Give the extent of all Plasmodium ovale-infected red blood cells.
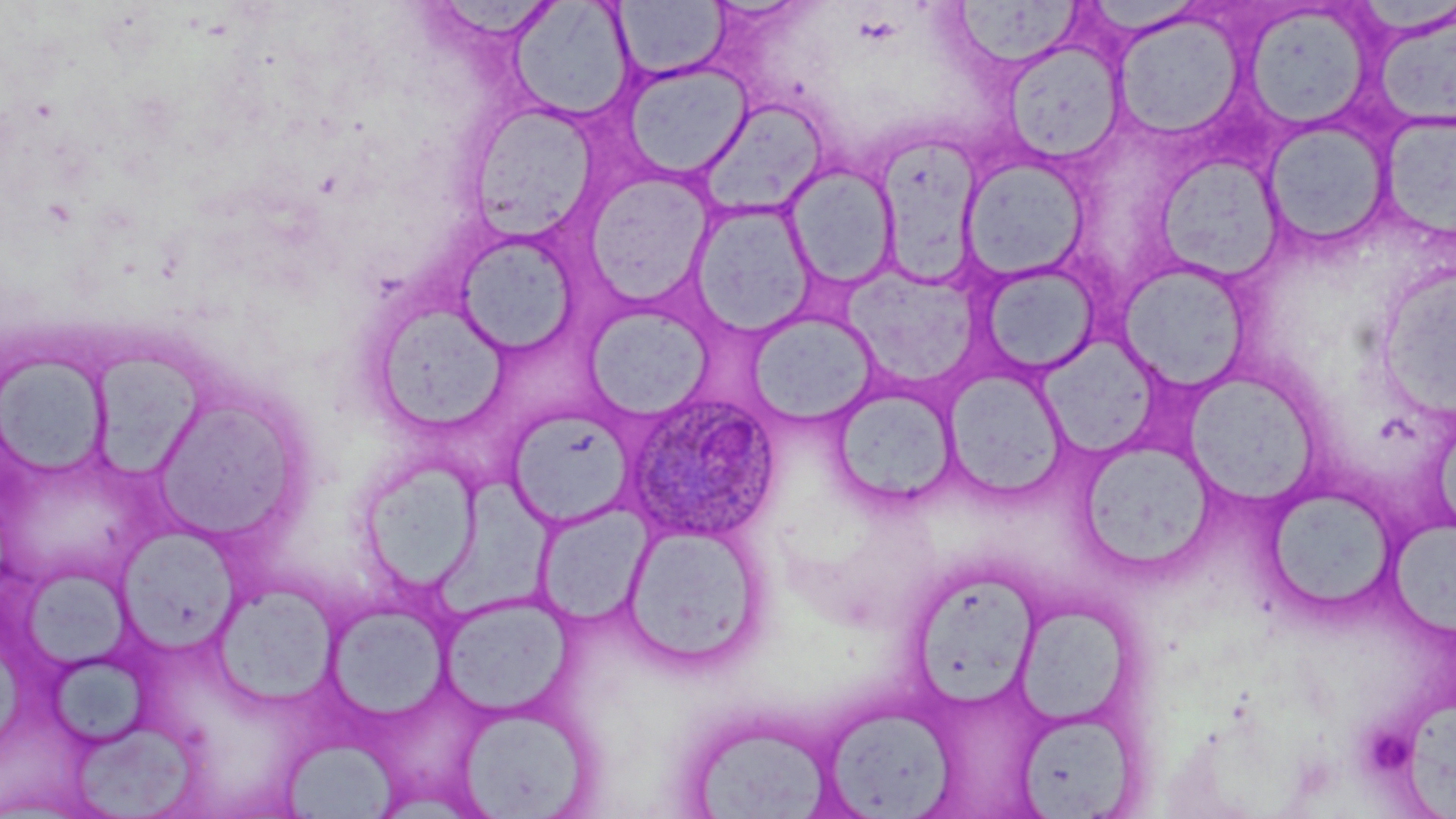

Approximate bounding boxes as (x1, y1, x2, y2) in pixels.
Plasmodium ovale-infected red blood cells: (617, 391, 782, 545).

slide-level diagnosis = Plasmodium ovale
preparation = thin blood smear
stain = May-Grünwald-Giemsa
field of view = single
magnification = 1000x
platelet locations = approximate bounding boxes as (x1, y1, x2, y2) in pixels: (1369, 733, 1413, 772)
uninfected red blood cell locations = approximate bounding boxes as (x1, y1, x2, y2) in pixels: (950, 0, 1087, 74), (508, 1, 635, 122), (613, 1, 729, 81), (1245, 5, 1372, 130), (1373, 9, 1456, 133), (1112, 14, 1245, 141), (1004, 39, 1125, 164), (621, 61, 752, 180), (699, 101, 828, 219), (468, 104, 603, 239), (1379, 111, 1455, 244), (1261, 119, 1394, 252), (878, 131, 985, 283), (1157, 154, 1282, 282), (961, 155, 1090, 280), (784, 163, 899, 290), (582, 169, 717, 306), (689, 201, 816, 336), (455, 233, 580, 357), (976, 261, 1102, 379), (1118, 261, 1252, 392), (843, 264, 982, 390), (1378, 266, 1455, 417), (369, 300, 511, 435), (583, 305, 713, 420), (748, 312, 878, 425), (0, 350, 112, 479), (86, 355, 209, 486), (943, 367, 1068, 498), (1186, 371, 1319, 507), (830, 383, 959, 508), (150, 388, 309, 546), (505, 409, 634, 529), (1079, 438, 1215, 574), (358, 454, 483, 593), (1263, 484, 1401, 616), (535, 502, 651, 625), (1390, 519, 1456, 637), (620, 522, 769, 670), (119, 530, 241, 656), (908, 564, 1042, 708), (29, 565, 137, 675), (215, 580, 341, 707), (439, 594, 573, 717), (1011, 597, 1140, 730), (322, 598, 454, 724), (50, 655, 151, 747), (1405, 688, 1456, 819), (455, 702, 598, 818), (819, 703, 960, 817), (1013, 708, 1142, 818), (76, 722, 197, 819), (689, 723, 828, 819), (281, 738, 406, 819)
image size = 1456×819 pixels
modality = light microscopy